Identify the cell.
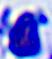

This is a leukocyte.

Summary:
  - Modality: micrograph
  - Magnification: 400x